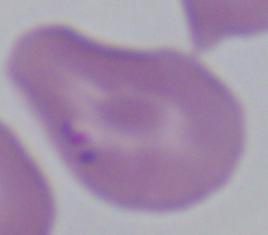

magnification: 1000x
identification: Babesia
modality: micrograph